Assess the morphology of the red blood cells.
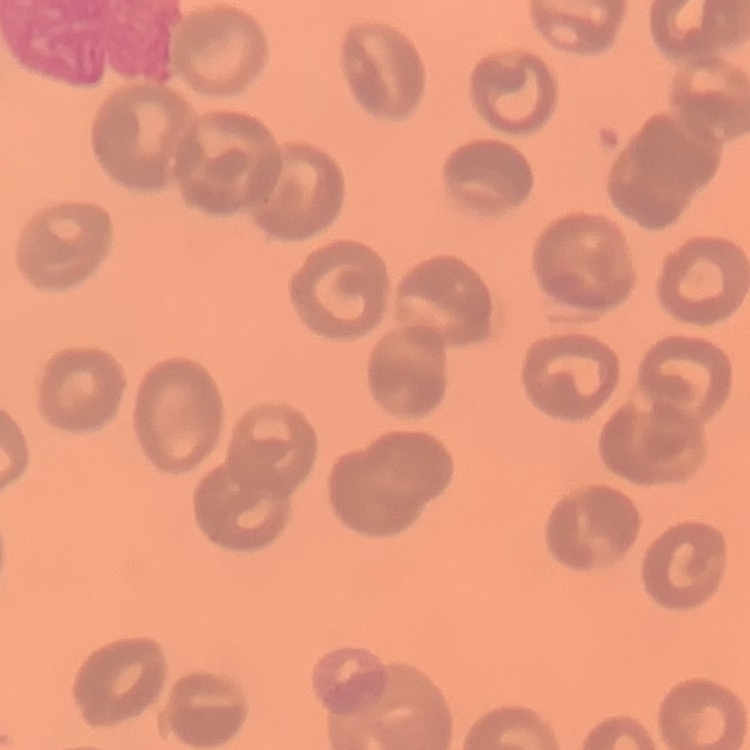

No rouleaux formation.

preparation = thin blood film
stain = Field's or Giemsa
image type = square crop of a larger photomicrograph